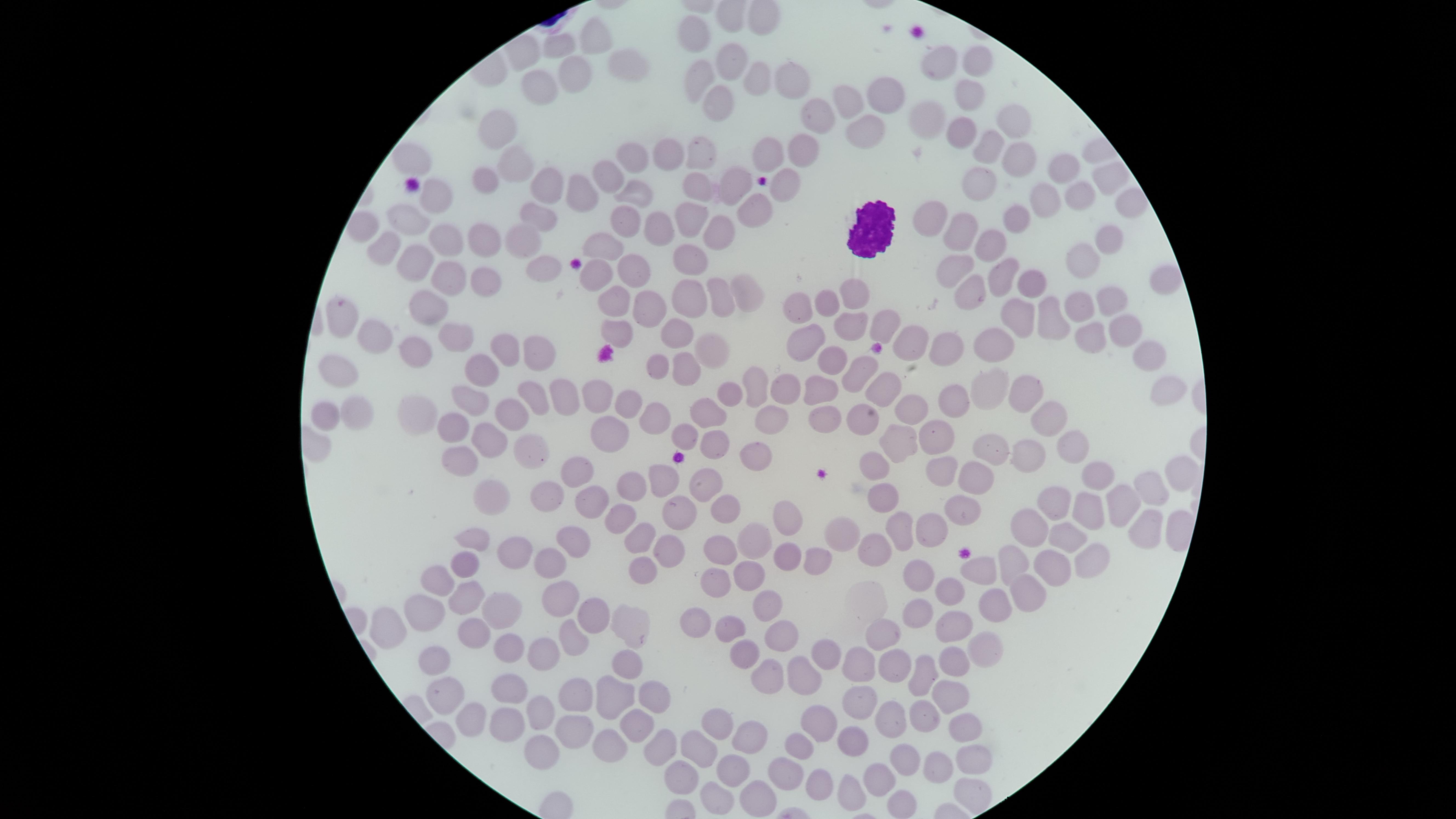
preparation = thin blood film
visible region = circular
uninfected red blood cells = approximate marker points as {x, y} in pixels: {599, 36}, {697, 36}, {561, 45}, {625, 62}, {980, 62}, {941, 63}, {727, 64}, {582, 71}, {699, 78}, {784, 78}, {750, 82}, {540, 87}, {965, 90}, {881, 93}, {714, 97}, {846, 99}, {820, 117}, {932, 119}, {1015, 124}, {860, 129}, {498, 130}, {966, 133}, {985, 148}, {766, 149}, {694, 152}, {802, 153}, {1016, 156}, {410, 157}, {626, 160}, {666, 160}, {517, 162}, {1058, 170}, {606, 177}, {1105, 180}, {483, 181}, {551, 183}, {737, 186}, {978, 190}, {583, 191}, {781, 191}, {695, 192}, {630, 195}, {1078, 195}, {442, 199}, {1039, 199}, {1130, 205}, {755, 211}, {543, 214}, {410, 217}, {617, 217}, {1014, 217}, {683, 218}, {926, 220}, {959, 224}, {654, 225}, {720, 231}, {481, 236}, {443, 237}, {1114, 240}, {522, 241}, {601, 242}, {386, 245}, {993, 247}, {690, 261}, {1080, 262}, {421, 263}, {543, 263}, {946, 265}, {629, 268}, {1005, 273}, {472, 274}, {593, 274}, {440, 275}, {1033, 281}, {1163, 281}, {742, 287}, {855, 295}, {973, 295}, {1105, 296}, {609, 297}, {689, 300}, {826, 301}, {431, 302}, {718, 303}, {1082, 304}, {639, 307}, {800, 311}, {345, 316}, {1017, 316}, {1049, 320}, {884, 325}, {849, 327}, {1125, 328}, {677, 331}, {613, 332}, {453, 333}, {1087, 336}, {373, 338}, {911, 340}, {508, 347}, {809, 347}, {991, 347}, {412, 350}, {714, 350}, {542, 352}, {946, 352}, {1150, 357}, {688, 365}, {658, 366}, {832, 367}, {337, 372}, {856, 373}, {483, 374}, {756, 381}, {824, 381}, {986, 386}, {559, 389}, {787, 389}, {876, 389}, {529, 390}, {589, 391}, {1022, 392}, {1158, 392}, {728, 394}, {466, 397}, {957, 400}, {623, 403}, {909, 405}, {706, 409}, {327, 410}, {350, 410}, {506, 413}, {415, 416}, {644, 417}, {826, 418}, {1052, 418}, {768, 421}, {861, 421}, {445, 425}, {609, 426}, {486, 431}, {685, 432}, {900, 439}, {940, 440}, {1068, 443}, {715, 444}, {529, 449}, {991, 452}, {1019, 452}, {756, 453}, {463, 457}, {872, 465}, {943, 468}, {574, 473}, {661, 475}, {1177, 475}, {1100, 478}, {637, 479}, {706, 480}, {972, 482}, {540, 491}, {1150, 491}, {884, 494}, {494, 495}, {1055, 497}, {599, 502}, {1123, 504}, {1083, 507}, {959, 509}, {723, 510}, {682, 511}, {619, 512}, {786, 512}, {1029, 513}, {1145, 525}, {927, 526}, {845, 527}, {898, 529}, {1057, 532}, {643, 534}, {474, 535}, {753, 538}, {569, 540}, {668, 545}, {876, 546}, {720, 552}, {513, 553}, {784, 559}, {1016, 559}, {1088, 560}, {810, 561}, {549, 562}, {469, 564}, {1052, 565}, {639, 566}, {979, 568}, {437, 576}, {711, 576}, {747, 576}, {914, 579}, {1021, 584}, {462, 589}, {945, 590}, {557, 595}, {768, 600}, {988, 606}, {496, 608}, {588, 611}, {423, 612}, {913, 616}, {695, 621}, {952, 621}, {394, 626}, {621, 627}, {727, 628}, {476, 629}, {775, 631}, {874, 637}, {573, 641}, {510, 647}, {743, 649}, {979, 649}, {544, 653}, {824, 653}, {434, 657}, {894, 659}, {623, 661}, {948, 663}, {855, 666}, {800, 676}, {922, 679}, {768, 682}, {507, 689}, {442, 692}, {578, 692}, {650, 692}, {949, 697}, {609, 698}, {856, 701}, {463, 712}, {538, 712}, {928, 714}, {891, 716}, {816, 721}, {716, 723}, {497, 725}, {637, 726}, {965, 728}, {570, 733}, {744, 734}, {851, 738}, {798, 741}, {701, 744}, {654, 745}, {538, 747}, {599, 748}, {965, 759}, {902, 760}, {933, 764}, {727, 768}, {789, 769}, {819, 776}, {677, 777}, {880, 779}, {843, 788}, {965, 791}, {757, 795}, {715, 802}
white blood cells = approximate marker points as {x, y} in pixels: {870, 226}
image size = 1456×819 pixels
capture = smartphone photograph through the microscope eyepiece
stain = Giemsa
field of view = single
presence = no malaria parasites detected